Locate and identify every blood parasite.
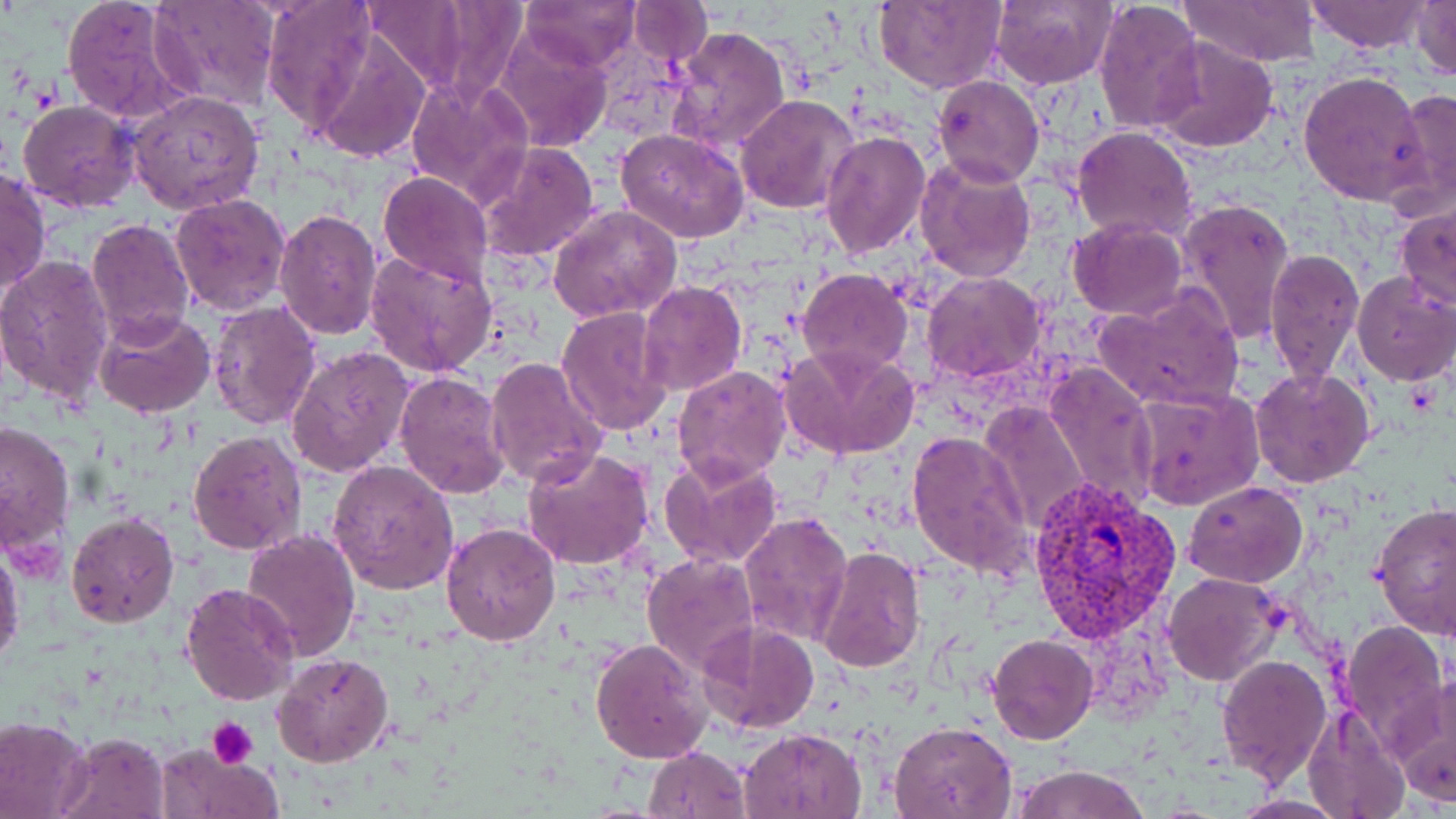
Approximate bounding boxes as (x1,y1)-(x2,y2) corner pairs in pixels.
Plasmodium vivax-infected red blood cells: (1027,476)-(1182,641).
No Plasmodium falciparum, Plasmodium ovale, Plasmodium malariae, Babesia divergens, or Trypanosoma brucei observed.

Summary:
  - Uninfected red blood cell locations: (60,0)-(198,127), (261,0)-(379,131), (517,0)-(639,72), (989,0)-(1114,90), (1093,0)-(1207,138), (1305,0)-(1430,52), (1340,0)-(1456,71), (1409,0)-(1456,79), (147,1)-(280,111), (627,1)-(711,62), (872,1)-(1006,92), (1183,1)-(1321,66), (360,3)-(481,93), (307,25)-(432,166), (489,25)-(613,153), (665,25)-(791,156), (1151,37)-(1279,153), (1298,70)-(1432,205), (933,74)-(1044,187), (405,75)-(533,207), (1391,87)-(1456,218), (127,91)-(265,214), (734,93)-(859,215), (18,100)-(141,212), (1072,126)-(1198,240), (616,128)-(751,243), (820,129)-(931,260), (476,141)-(600,262), (915,153)-(1037,283), (1,167)-(50,301), (378,172)-(492,286), (169,193)-(291,315), (1174,198)-(1295,348), (1394,204)-(1454,310), (548,205)-(682,325), (275,207)-(384,342), (85,216)-(195,344), (1067,219)-(1188,320), (1265,246)-(1365,389), (363,250)-(497,377), (0,254)-(115,408), (797,268)-(912,376), (921,272)-(1045,383), (1351,272)-(1456,386), (638,280)-(747,396), (1093,288)-(1245,412), (207,299)-(322,430), (556,305)-(672,437), (95,310)-(218,419), (779,341)-(921,461), (285,345)-(416,480), (484,355)-(608,490), (1045,362)-(1159,511), (673,364)-(791,484), (1250,367)-(1375,488), (394,371)-(509,501), (1132,387)-(1262,510), (980,400)-(1089,531), (0,418)-(76,563), (188,430)-(304,555), (906,430)-(1033,580), (521,448)-(657,571), (659,453)-(786,570), (327,460)-(459,595), (1182,480)-(1309,586), (1371,502)-(1456,638), (66,511)-(179,627), (738,511)-(853,650), (440,521)-(561,645), (242,528)-(362,664), (0,541)-(25,674), (813,546)-(924,675), (640,553)-(760,676), (1161,571)-(1283,685), (179,583)-(301,707), (1337,619)-(1450,753), (697,620)-(820,734), (987,634)-(1097,744), (589,637)-(710,765), (273,652)-(395,769), (1216,653)-(1333,786), (1390,678)-(1456,807), (1302,703)-(1411,819), (0,716)-(94,818), (890,719)-(1019,818), (740,728)-(867,819), (57,730)-(170,819), (152,743)-(281,818), (644,746)-(751,818), (1011,764)-(1149,819), (1229,793)-(1350,817)
  - Platelet locations: (206,717)-(258,768)
  - Slide-level diagnosis: Plasmodium vivax
  - Magnification: 1000x
  - Image size: 1456×819 pixels
  - Modality: light microscopy
  - Preparation: thin blood film
  - Stain: May-Grünwald-Giemsa
  - Field of view: single